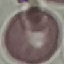
Result: no malaria parasites detected. Photographed with a smartphone camera at the microscope eyepiece. Giemsa stain. Automatically extracted cell patch, resized to 64 × 64 pixels. Thin blood film.